Locate Plasmodium parasites and leukocytes.
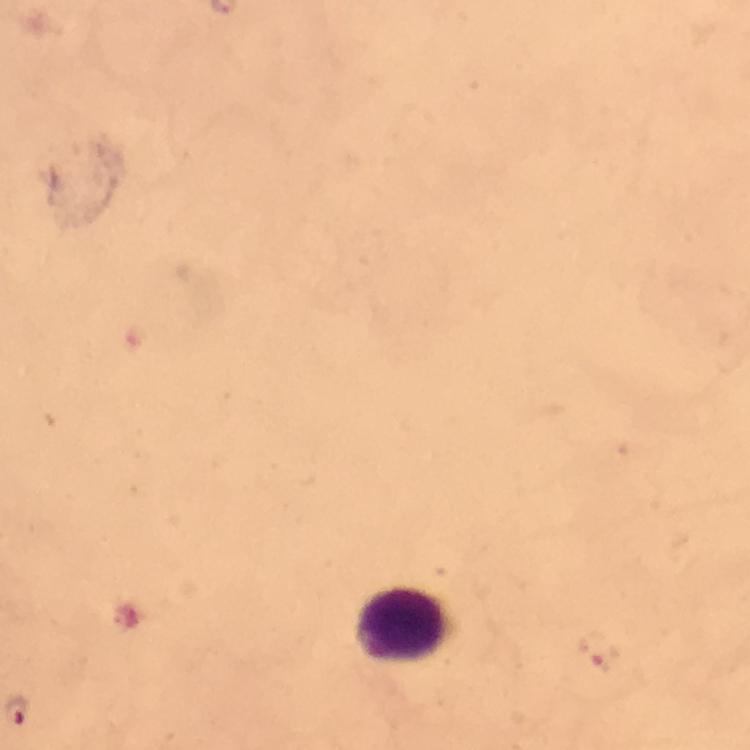

Approximate centers as [x, y] in pixels.
Plasmodium parasites: [600, 650].
Leukocytes: [402, 627].

capture: smartphone photograph through a microscope
image_size: 750×750 pixels
stain: Giemsa
immersion_oil: used
preparation: thick blood smear
context: from a diagnostic examination for malaria
cropped_from: one field of view
magnification: 100x